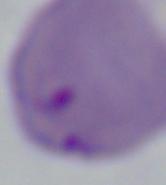
modality = micrograph
identification = Babesia
magnification = 1000x